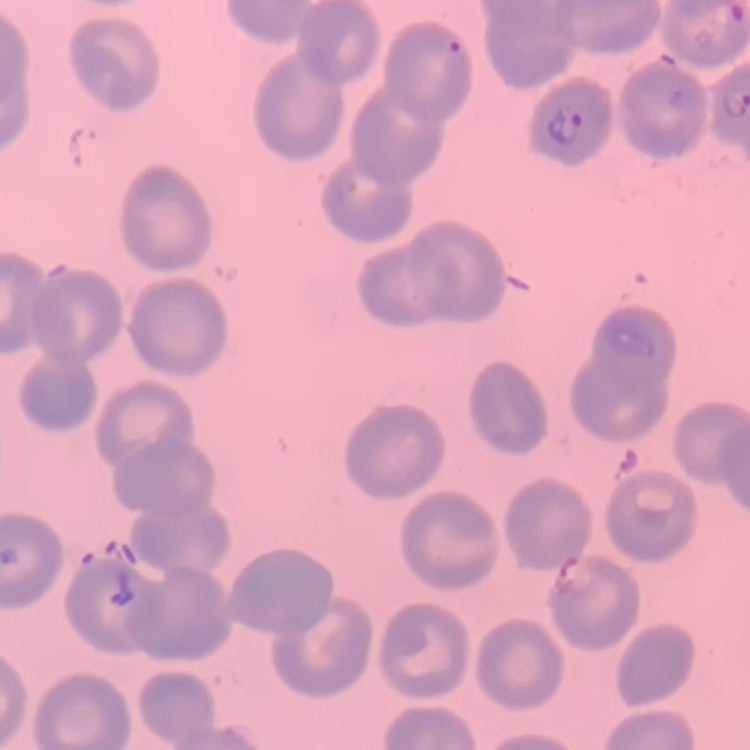
erythrocyte morphology = no rouleaux formation
stain = Field's or Giemsa
preparation = thin blood film
image type = one tile cut from a larger photomicrograph